Report the malaria status of this cell.
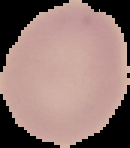

It is uninfected.

From a thin blood film. Image is 130×148 pixels. Segmented cell region on a black background.